Classify this cell by malaria status.
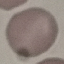
Uninfected.

Giemsa-stained preparation. Photographed with a smartphone camera at the microscope eyepiece. Thin smear of blood. Cell patch, automatically extracted from a larger field of view and resized to 64 × 64 pixels.